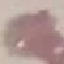 Malaria status: uninfected. Automatically extracted cell patch, resized to 64 × 64 pixels. Photographed with a smartphone camera at the microscope eyepiece. Giemsa-stained preparation. Thin blood film.